Locate and identify every blood parasite.
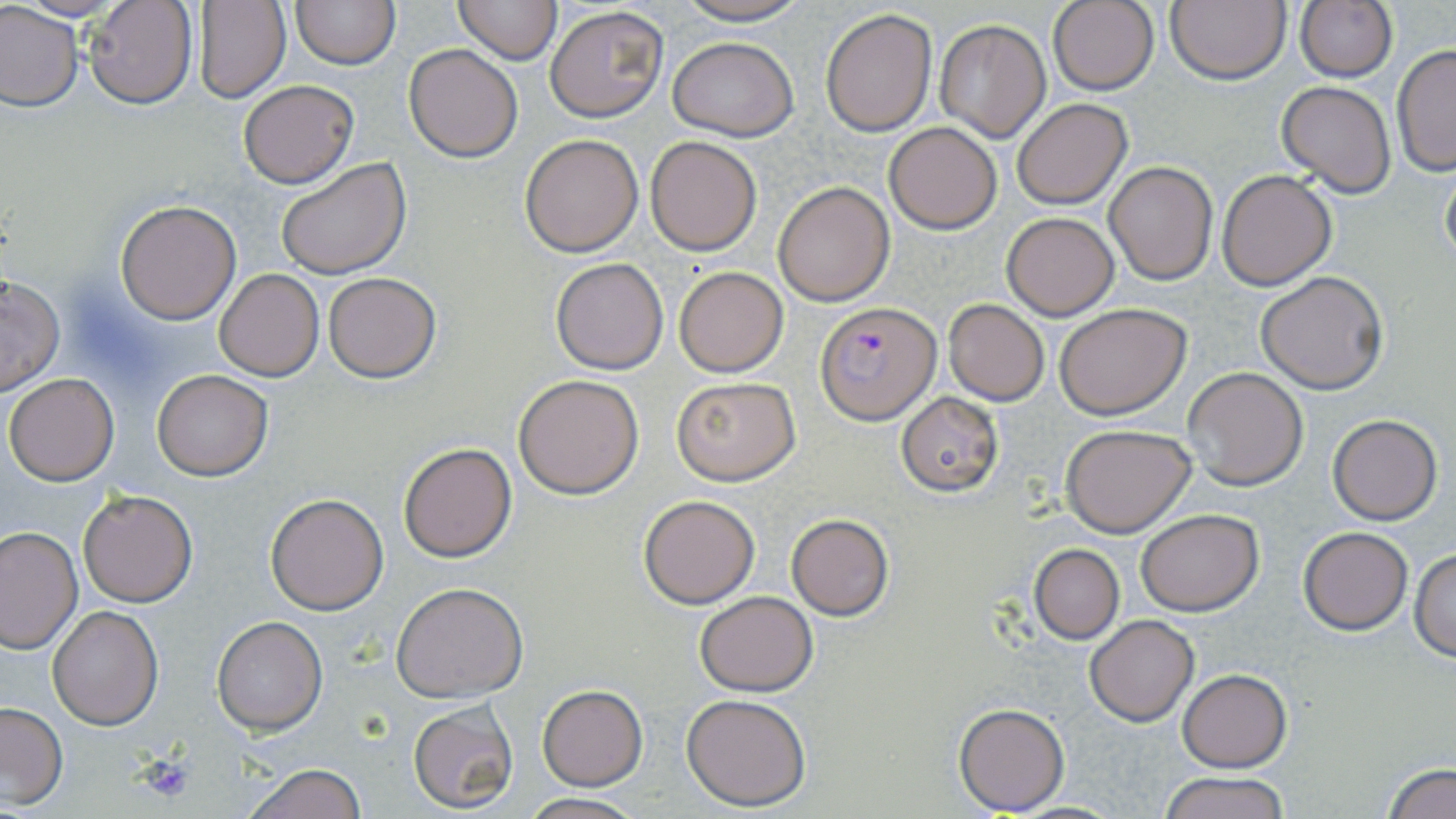
Approximate bounding boxes as (x1,y1)-(x2,y2) corner pairs in pixels.
Plasmodium falciparum-infected red blood cells: (816,302)-(941,425).
No Plasmodium ovale, Plasmodium malariae, Plasmodium vivax, Babesia divergens, or Trypanosoma brucei observed.

Summary:
  - Uninfected red blood cell locations: (82,0)-(198,109), (290,0)-(398,70), (453,0)-(560,64), (666,0)-(814,26), (1166,0)-(1290,84), (1295,0)-(1397,83), (1046,1)-(1160,96), (192,2)-(289,102), (0,4)-(80,111), (543,4)-(667,122), (821,8)-(938,138), (933,18)-(1052,141), (667,34)-(799,142), (1391,43)-(1456,178), (405,44)-(524,162), (237,79)-(359,187), (1276,80)-(1397,198), (1011,99)-(1132,208), (883,121)-(1002,233), (519,133)-(645,257), (643,136)-(763,256), (275,157)-(411,280), (1439,159)-(1456,269), (1104,161)-(1218,284), (1216,169)-(1337,290), (773,182)-(895,306), (114,199)-(242,323), (1002,212)-(1119,320), (551,257)-(670,374), (674,267)-(788,376), (213,268)-(323,381), (1255,271)-(1389,393), (323,273)-(443,383), (0,274)-(64,395), (942,299)-(1050,405), (1054,303)-(1192,419), (1181,367)-(1308,492), (151,369)-(273,480), (5,372)-(120,486), (513,373)-(644,499), (672,377)-(800,484), (896,393)-(1003,495), (1328,414)-(1442,525), (1060,424)-(1197,536), (398,441)-(517,563), (78,489)-(198,608), (266,493)-(389,615), (638,494)-(761,608), (1136,508)-(1263,615), (786,513)-(894,621), (0,526)-(82,656), (1298,526)-(1413,635), (1029,544)-(1125,643), (1410,547)-(1456,660), (391,581)-(530,702), (694,591)-(819,694), (47,604)-(164,730), (1084,613)-(1198,726), (211,615)-(327,735), (1177,669)-(1290,772), (536,685)-(649,790), (681,692)-(811,810), (408,701)-(519,814), (0,702)-(68,808), (954,702)-(1070,815), (239,762)-(367,819), (1383,762)-(1456,819), (1158,772)-(1293,819), (520,793)-(644,819)
  - Platelet locations: (138,754)-(198,803)
  - Slide-level diagnosis: Plasmodium falciparum
  - Stain: May-Grünwald-Giemsa
  - Magnification: 1000x
  - Modality: optical microscopy
  - Preparation: thin blood smear
  - Image size: 1456×819 pixels
  - Field of view: single